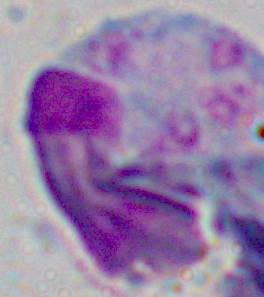

{
  "modality": "micrograph",
  "identification": "leukocyte",
  "magnification": "1000x"
}